State the blood parasite species.
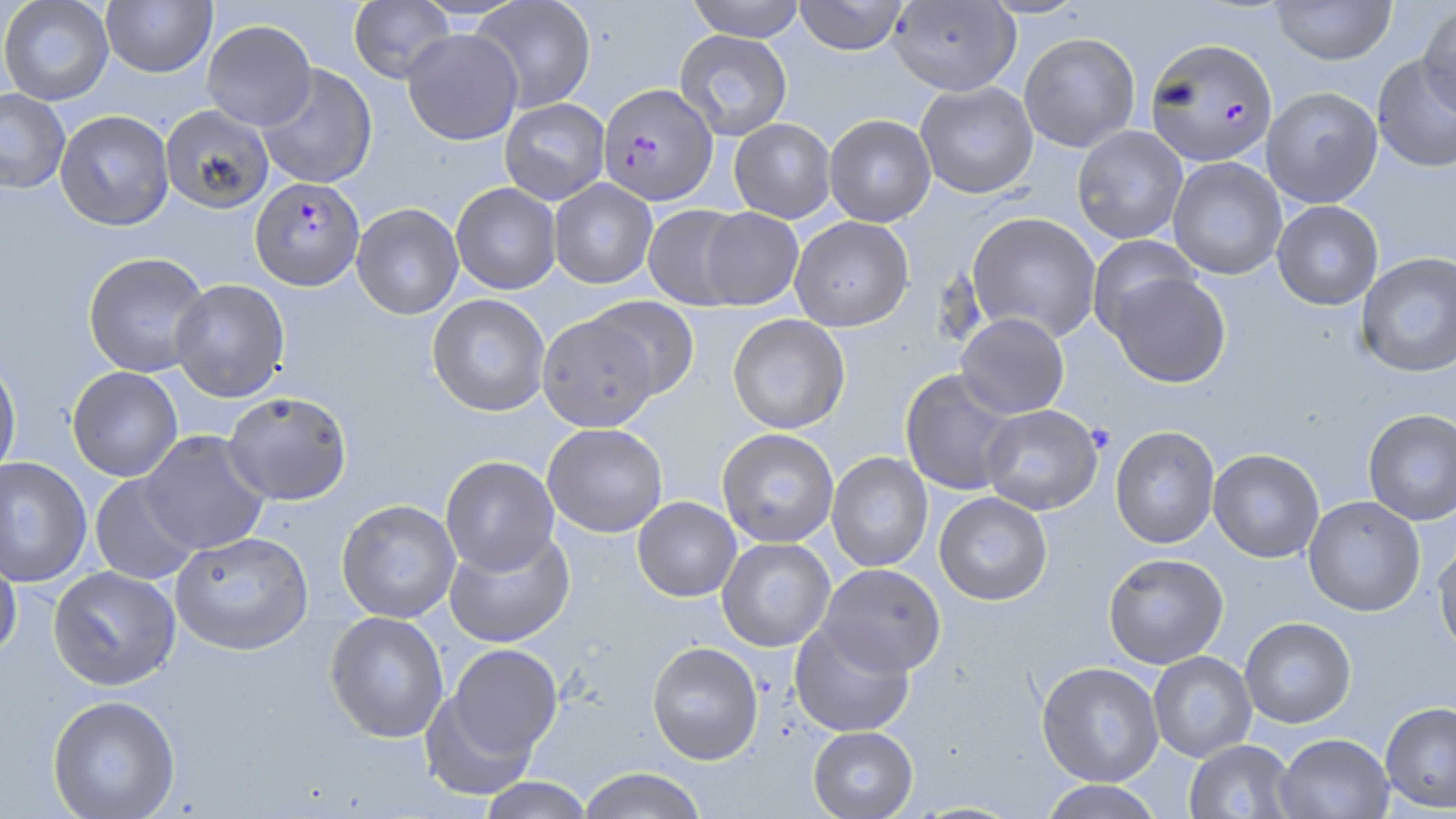
Plasmodium falciparum.

stain = May-Grünwald-Giemsa
field of view = one of a larger specimen
modality = light microscopy
uninfected red blood cell locations = approximate bounding boxes as [x1, y1, x2, y2] in pixels: [1, 0, 114, 105], [101, 0, 216, 77], [348, 0, 455, 83], [470, 0, 597, 113], [684, 0, 808, 41], [794, 0, 910, 56], [887, 0, 1021, 96], [1269, 1, 1397, 66], [1417, 2, 1456, 118], [202, 20, 316, 130], [402, 28, 523, 145], [674, 30, 793, 140], [1019, 32, 1141, 152], [1372, 55, 1456, 173], [256, 65, 378, 189], [915, 81, 1038, 199], [1261, 87, 1383, 207], [0, 89, 70, 194], [500, 98, 610, 204], [159, 105, 275, 214], [55, 110, 174, 231], [823, 114, 936, 226], [728, 118, 836, 222], [1072, 126, 1188, 244], [1168, 157, 1287, 279], [549, 179, 657, 289], [451, 183, 562, 295], [1272, 201, 1384, 310], [351, 204, 463, 320], [642, 204, 752, 310], [698, 208, 803, 311], [966, 212, 1101, 341], [789, 216, 914, 331], [1087, 236, 1203, 342], [1355, 251, 1456, 378], [82, 252, 211, 377], [1103, 269, 1231, 388], [170, 279, 290, 403], [426, 295, 550, 417], [587, 298, 700, 401], [537, 313, 660, 432], [955, 313, 1070, 419], [727, 314, 851, 433], [0, 357, 22, 480], [67, 367, 183, 482], [899, 370, 1021, 496], [222, 392, 353, 506], [981, 405, 1103, 515], [1363, 409, 1456, 525], [543, 424, 668, 537], [1109, 427, 1220, 549], [717, 428, 839, 548], [140, 431, 270, 555], [1208, 449, 1325, 563], [826, 453, 933, 572], [440, 456, 559, 576], [0, 457, 92, 587], [89, 474, 201, 585], [934, 492, 1053, 606], [1303, 497, 1426, 617], [632, 498, 742, 602], [335, 500, 461, 623], [444, 531, 576, 648], [170, 532, 314, 658], [716, 538, 835, 652], [1432, 542, 1456, 659], [0, 551, 22, 663], [1103, 553, 1229, 669], [818, 564, 946, 676], [47, 567, 181, 693], [324, 612, 449, 744], [1239, 617, 1356, 728], [790, 621, 915, 736], [646, 642, 764, 765], [446, 644, 562, 764], [1149, 652, 1256, 761], [1036, 662, 1164, 787], [419, 690, 539, 802], [47, 698, 181, 819], [1380, 703, 1456, 813], [807, 726, 918, 819], [1274, 734, 1393, 819], [1183, 740, 1297, 819], [577, 768, 708, 819], [477, 777, 595, 819], [1037, 780, 1165, 819]
Plasmodium falciparum-infected red blood cell locations = approximate bounding boxes as [x1, y1, x2, y2] in pixels: [1143, 39, 1279, 169], [599, 84, 718, 206], [250, 177, 364, 292]
preparation = thin blood film
image size = 1456×819 pixels
magnification = 1000x